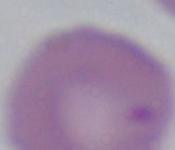 A Babesia parasite is shown. 1000x magnification. Micrograph.